Name the blood parasite species.
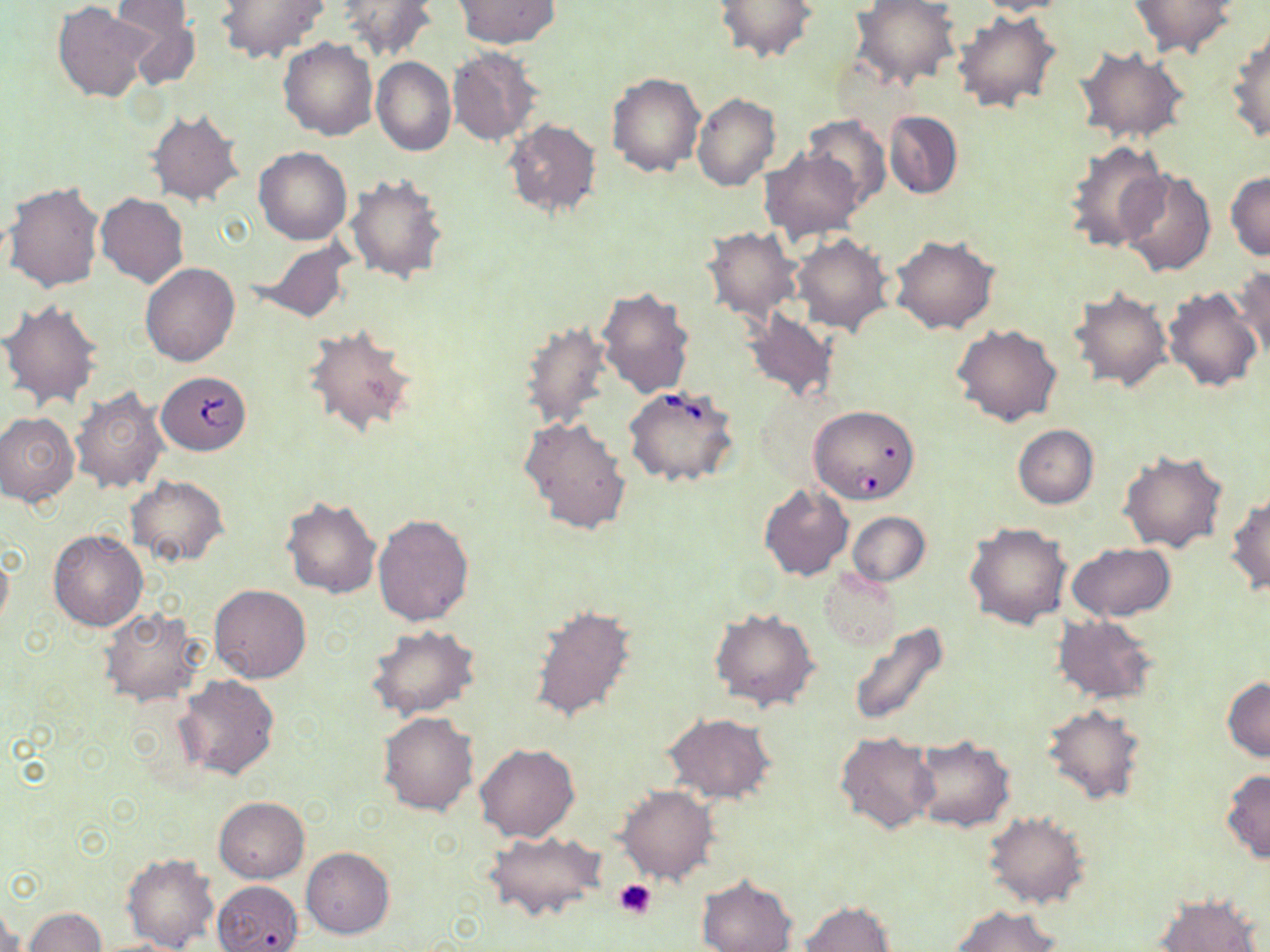

Babesia divergens.

Approximate bounding boxes as [x1, y1, x2, y2] in pixels. Platelet locations: [612, 879, 658, 920]. Babesia divergens-infected red blood cell locations: [154, 373, 251, 457], [623, 384, 740, 488], [805, 411, 917, 506]. Uninfected red blood cell locations: [215, 0, 327, 64], [336, 0, 440, 62], [714, 0, 818, 64], [851, 0, 960, 90], [972, 0, 1076, 16], [110, 1, 197, 57], [454, 1, 559, 49], [1127, 1, 1237, 58], [53, 2, 153, 103], [952, 9, 1062, 114], [1227, 28, 1270, 144], [279, 38, 378, 140], [448, 46, 541, 146], [1073, 46, 1191, 145], [372, 57, 456, 156], [605, 72, 705, 178], [691, 92, 780, 192], [148, 108, 245, 208], [884, 110, 962, 199], [802, 116, 890, 204], [502, 118, 602, 219], [1063, 140, 1171, 253], [254, 146, 353, 245], [758, 149, 864, 241], [1118, 170, 1217, 277], [1226, 171, 1270, 259], [345, 173, 450, 285], [4, 180, 106, 292], [96, 193, 189, 288], [702, 227, 805, 323], [791, 234, 893, 336], [890, 234, 998, 335], [249, 238, 353, 323], [140, 264, 240, 366], [1231, 265, 1270, 363], [596, 286, 696, 399], [1165, 286, 1264, 393], [1068, 287, 1172, 392], [0, 300, 105, 410], [743, 309, 839, 404], [519, 317, 613, 431], [301, 324, 420, 440], [952, 324, 1062, 427], [70, 387, 168, 494], [0, 409, 80, 506], [518, 416, 632, 536], [1014, 424, 1099, 509], [1118, 451, 1229, 554], [126, 474, 229, 567], [758, 484, 853, 581], [1227, 494, 1270, 595], [280, 496, 381, 599], [848, 512, 929, 585], [372, 513, 474, 625], [966, 522, 1071, 628], [49, 531, 147, 631], [1067, 543, 1176, 621], [0, 547, 12, 632], [820, 569, 901, 650], [209, 584, 311, 682], [527, 602, 637, 725], [99, 608, 205, 706], [711, 610, 819, 712], [1052, 613, 1159, 706], [847, 623, 949, 730], [367, 624, 479, 720], [174, 674, 281, 780], [1223, 677, 1270, 762], [1041, 705, 1145, 806], [377, 712, 479, 815], [662, 714, 775, 802], [835, 732, 937, 834], [909, 737, 1013, 832], [474, 743, 579, 842], [1221, 769, 1270, 862], [619, 786, 717, 885], [213, 797, 309, 883], [985, 812, 1088, 909], [483, 828, 608, 924], [301, 847, 395, 938], [121, 852, 217, 952], [696, 875, 798, 951], [213, 879, 303, 952], [1154, 893, 1263, 952], [0, 901, 22, 952], [800, 902, 898, 951], [952, 905, 1061, 952], [24, 907, 107, 951]. Single field of view. Image is 1270×952 pixels. Light microscopy. Captured at 1000x magnification. May-Grünwald-Giemsa-stained preparation. Thin blood film.